Name the parasite shown.
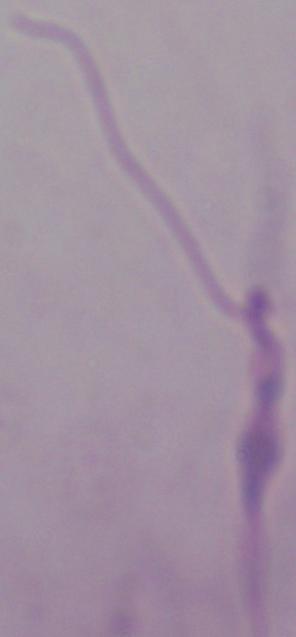

This is Leishmania.

Summary:
  - Magnification: 1000x
  - Modality: photomicrograph